Assess the morphology of the red blood cells.
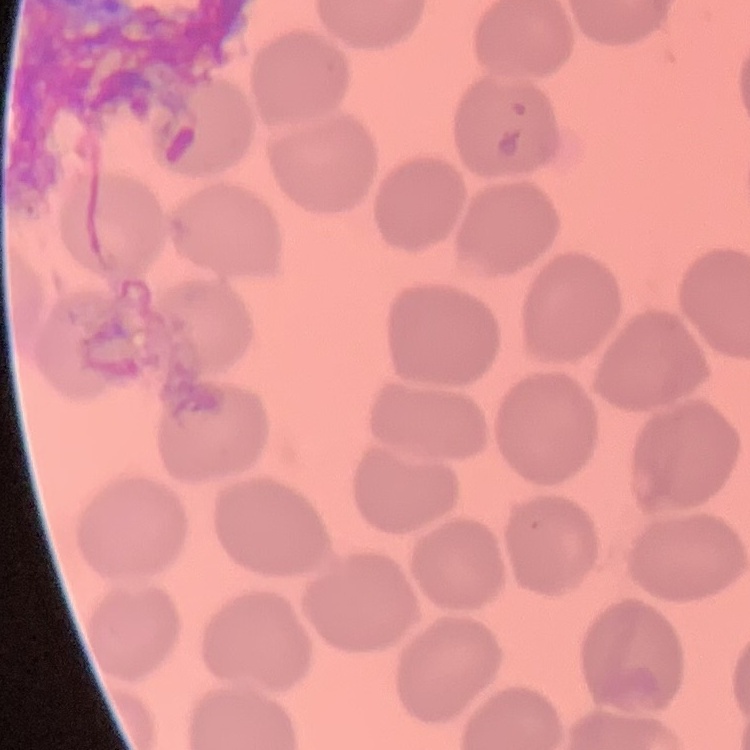
They show no rouleaux formation.

stain = Field's or Giemsa
preparation = thin peripheral smear
image type = square crop of a larger photomicrograph